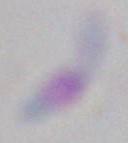

identification = Toxoplasma gondii
magnification = 1000x
modality = micrograph